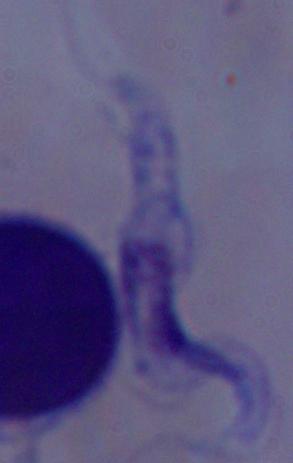 1000x magnification. A trypanosome is seen. Photomicrograph.